Classify this cell by malaria status.
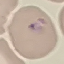
It is parasitized.

Summary:
  - Preparation: thin blood film
  - Image type: cell patch, automatically extracted from a larger field of view and resized to 64 × 64 pixels
  - Stain: Giemsa
  - Capture: smartphone camera at the microscope eyepiece